Point out each leukocyte.
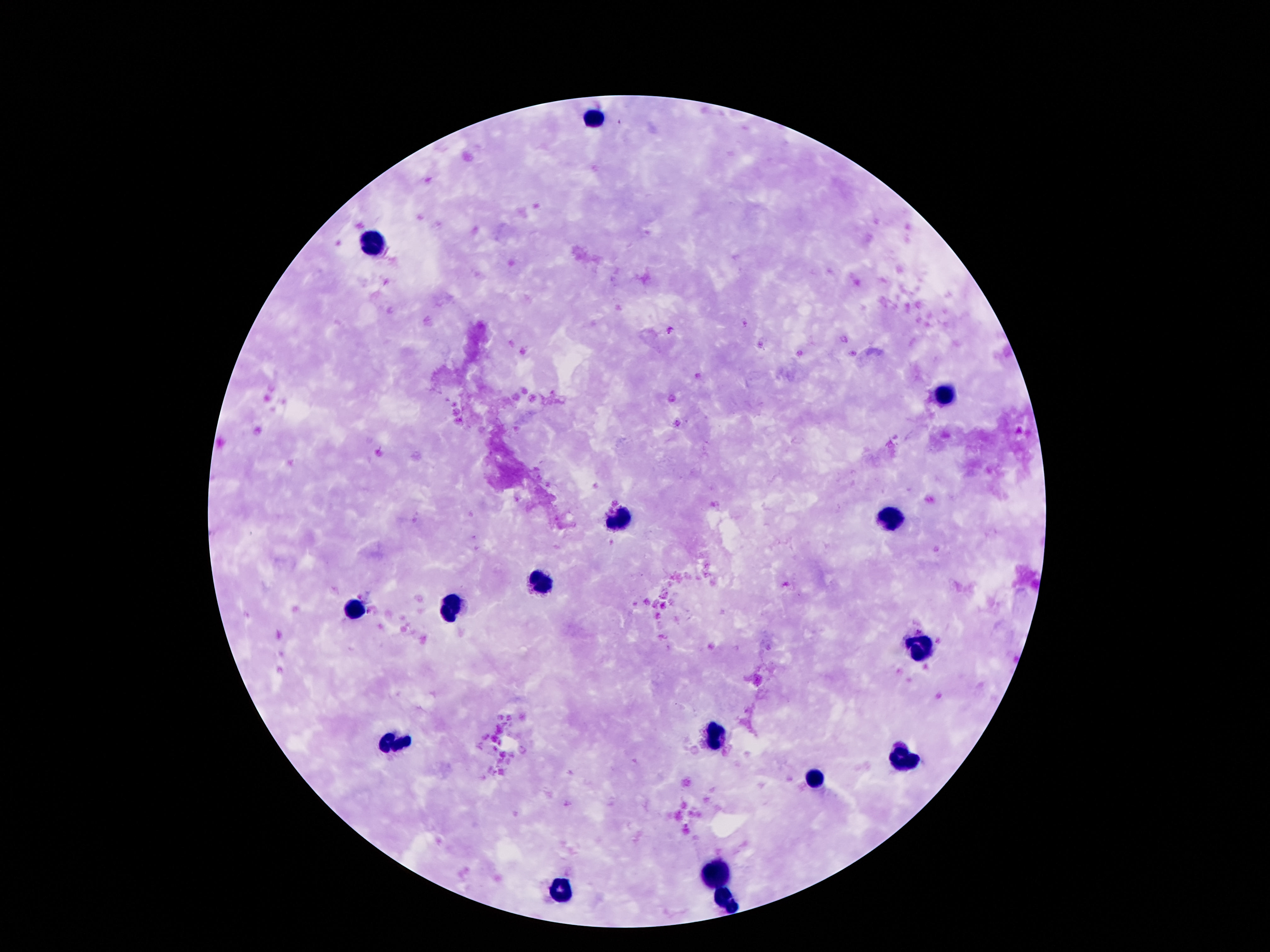
Approximate centers as [x, y] in pixels.
Leukocytes: [595, 118], [376, 246], [943, 396], [892, 520], [618, 522], [540, 582], [452, 606], [356, 610], [919, 647], [718, 737], [393, 744], [903, 758], [812, 780], [710, 874], [556, 891], [724, 899].

Patient malaria status: negative. Giemsa stain. Image is 1270×952 pixels. Single field of view. Smartphone photograph taken through the microscope eyepiece. 100x magnification. Thick blood film.